Give the extent of all Plasmodium falciparum-infected red blood cells.
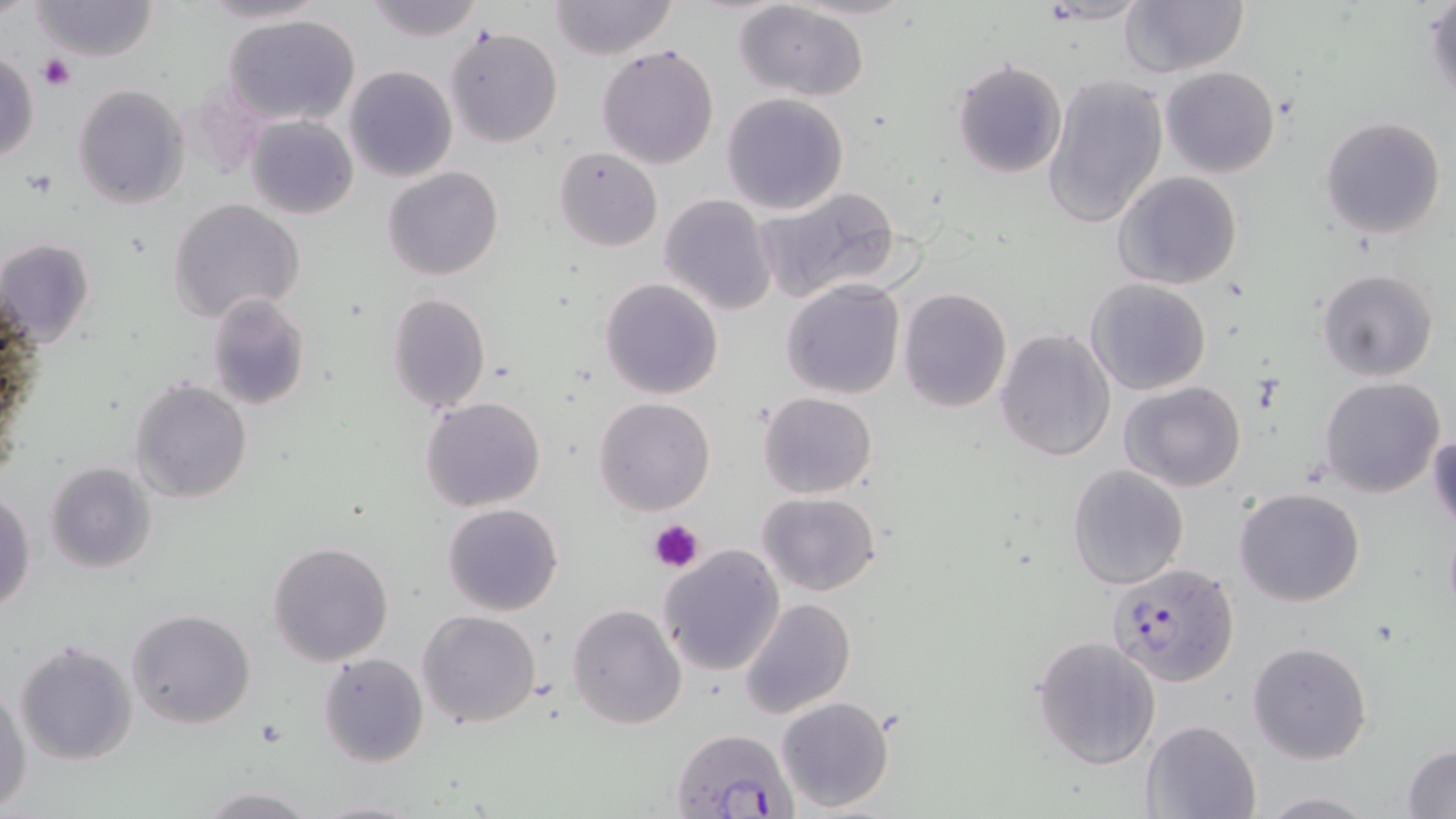

Approximate bounding boxes as named x1/y1/x2/y2 corners in pixels.
Plasmodium falciparum-infected red blood cells: (x1=1107, y1=561, x2=1240, y2=684), (x1=668, y1=725, x2=798, y2=819).

Summary:
  - Uninfected red blood cell locations: (x1=29, y1=0, x2=159, y2=62), (x1=194, y1=0, x2=331, y2=26), (x1=361, y1=0, x2=485, y2=43), (x1=547, y1=0, x2=681, y2=60), (x1=1033, y1=1, x2=1152, y2=25), (x1=1118, y1=1, x2=1251, y2=78), (x1=734, y1=2, x2=872, y2=101), (x1=1424, y1=2, x2=1455, y2=102), (x1=222, y1=12, x2=365, y2=126), (x1=444, y1=26, x2=563, y2=147), (x1=597, y1=43, x2=720, y2=171), (x1=0, y1=48, x2=40, y2=164), (x1=952, y1=59, x2=1068, y2=179), (x1=344, y1=65, x2=458, y2=183), (x1=1159, y1=65, x2=1281, y2=178), (x1=1042, y1=72, x2=1167, y2=229), (x1=73, y1=83, x2=191, y2=209), (x1=721, y1=91, x2=849, y2=215), (x1=245, y1=113, x2=359, y2=219), (x1=1321, y1=115, x2=1447, y2=239), (x1=555, y1=146, x2=662, y2=251), (x1=383, y1=166, x2=504, y2=280), (x1=1113, y1=170, x2=1243, y2=291), (x1=756, y1=185, x2=904, y2=302), (x1=658, y1=194, x2=777, y2=316), (x1=167, y1=198, x2=305, y2=323), (x1=0, y1=238, x2=96, y2=348), (x1=1315, y1=269, x2=1439, y2=382), (x1=1085, y1=277, x2=1211, y2=396), (x1=599, y1=278, x2=725, y2=401), (x1=781, y1=279, x2=906, y2=400), (x1=897, y1=288, x2=1012, y2=413), (x1=385, y1=291, x2=492, y2=415), (x1=204, y1=293, x2=312, y2=412), (x1=994, y1=327, x2=1117, y2=462), (x1=1318, y1=377, x2=1445, y2=498), (x1=129, y1=380, x2=253, y2=502), (x1=1120, y1=382, x2=1246, y2=492), (x1=757, y1=392, x2=878, y2=498), (x1=421, y1=396, x2=545, y2=512), (x1=592, y1=397, x2=716, y2=517), (x1=1429, y1=426, x2=1456, y2=532), (x1=44, y1=461, x2=157, y2=573), (x1=1067, y1=464, x2=1189, y2=589), (x1=0, y1=488, x2=36, y2=613), (x1=1234, y1=488, x2=1366, y2=607), (x1=756, y1=490, x2=881, y2=598), (x1=443, y1=503, x2=564, y2=616), (x1=267, y1=540, x2=395, y2=667), (x1=657, y1=544, x2=786, y2=676), (x1=737, y1=598, x2=856, y2=719), (x1=567, y1=603, x2=688, y2=730), (x1=126, y1=608, x2=257, y2=730), (x1=418, y1=610, x2=542, y2=730), (x1=1031, y1=634, x2=1162, y2=771), (x1=14, y1=639, x2=139, y2=765), (x1=1247, y1=640, x2=1373, y2=764), (x1=318, y1=653, x2=429, y2=767), (x1=0, y1=683, x2=31, y2=816), (x1=774, y1=696, x2=895, y2=813), (x1=1142, y1=719, x2=1261, y2=819), (x1=1402, y1=742, x2=1455, y2=819), (x1=196, y1=786, x2=320, y2=818), (x1=1255, y1=792, x2=1379, y2=817), (x1=311, y1=797, x2=427, y2=819)
  - Platelet locations: (x1=38, y1=54, x2=76, y2=92), (x1=25, y1=168, x2=58, y2=195), (x1=649, y1=519, x2=705, y2=573)
  - Slide-level diagnosis: Plasmodium falciparum
  - Image size: 1456×819 pixels
  - Field of view: single
  - Stain: May-Grünwald-Giemsa
  - Magnification: 1000x
  - Modality: optical microscopy
  - Preparation: thin blood smear